Identify the parasite.
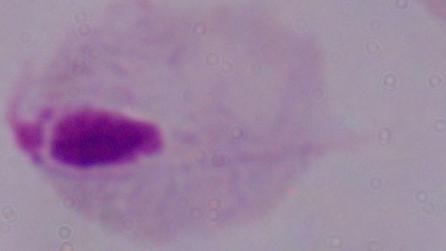
This is a trichomonad.

magnification = 1000x
modality = micrograph